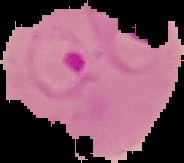
{
  "result": "Plasmodium parasites detected",
  "image_type": "segmented cell region on a black background",
  "preparation": "thin blood film",
  "image_size": "184×163 pixels"
}